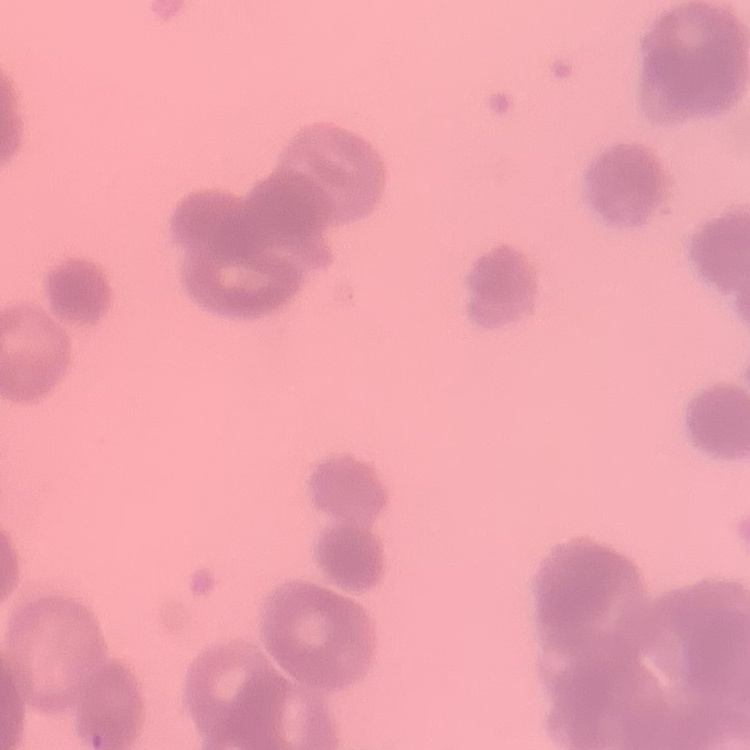

The red blood cells exhibit rouleaux formation. Square crop of a larger photomicrograph. Thin blood smear. Field's or Giemsa stain.